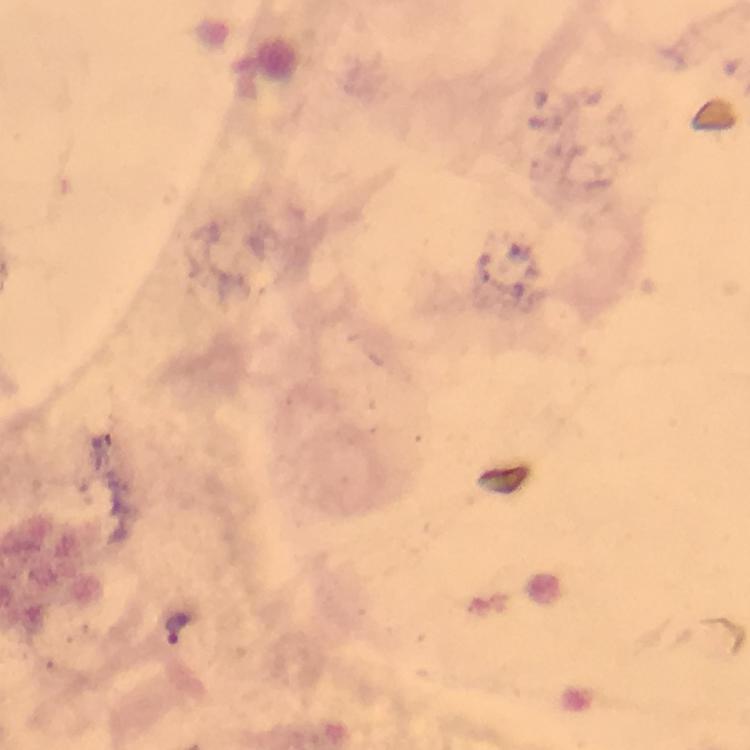
Approximate centers as {x, y} in pixels.
Summary:
  - Plasmodium parasite locations: {178, 625}
  - Magnification: 100x
  - Image size: 750×750 pixels
  - Immersion oil: applied
  - Context: from a malaria diagnostic workup
  - Capture: smartphone camera through the microscope
  - Cropped from: one field of view
  - Preparation: thick smear
  - Stain: Giemsa